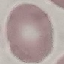

Summary:
  - Result: no malaria parasites detected
  - Preparation: thin blood film
  - Stain: Giemsa
  - Image type: cell patch, automatically extracted from a larger field of view and resized to 64 × 64 pixels
  - Capture: smartphone through the microscope eyepiece